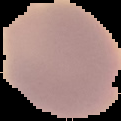

Malaria status: uninfected. From a thin blood film. Image is 121×121 pixels. Segmented cell region on a black background.